Identify the blood parasite species.
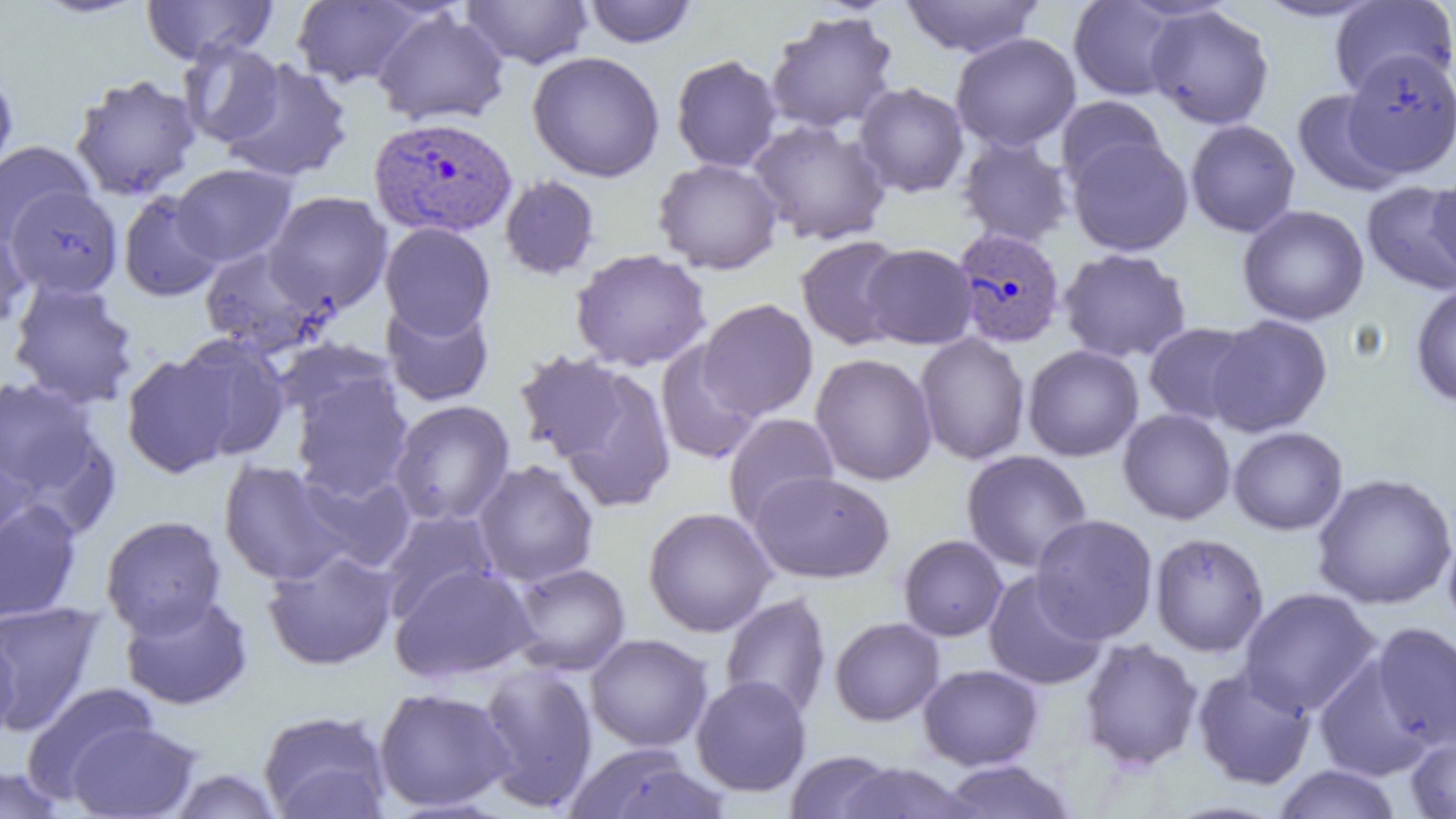
Plasmodium vivax.

Summary:
  - Coordinate format: approximate bounding boxes as (x1,y1)-(x2,y2) corner pairs in pixels
  - Uninfected red blood cell locations: (27,0)-(151,19), (140,0)-(278,65), (291,0)-(427,89), (460,0)-(594,69), (900,0)-(1044,58), (1250,0)-(1387,22), (584,1)-(698,48), (1068,1)-(1185,101), (1329,1)-(1456,98), (1145,4)-(1275,130), (371,9)-(510,127), (765,11)-(899,135), (950,33)-(1081,152), (179,39)-(286,148), (527,50)-(665,182), (1342,51)-(1455,177), (671,54)-(782,173), (220,59)-(353,182), (0,69)-(18,184), (70,74)-(202,201), (854,82)-(969,197), (1292,89)-(1405,196), (1056,95)-(1165,189), (1185,119)-(1300,238), (748,120)-(891,245), (958,136)-(1074,246), (1067,137)-(1194,256), (0,140)-(94,249), (653,158)-(783,274), (171,163)-(297,267), (1427,169)-(1456,283), (499,175)-(600,281), (1361,181)-(1456,296), (4,188)-(126,298), (118,191)-(223,302), (264,191)-(393,315), (1237,204)-(1369,326), (0,216)-(32,334), (380,223)-(496,339), (795,235)-(909,350), (861,243)-(977,349), (199,247)-(326,356), (570,248)-(712,371), (1058,248)-(1192,363), (8,279)-(140,409), (1410,282)-(1456,408), (698,298)-(818,421), (381,299)-(494,407), (1206,314)-(1333,437), (1143,322)-(1255,425), (915,333)-(1031,465), (173,334)-(291,460), (273,338)-(398,429), (655,341)-(763,465), (1023,344)-(1144,461), (513,350)-(630,463), (121,352)-(239,478), (810,353)-(938,486), (558,368)-(677,513), (292,374)-(413,501), (0,376)-(107,507), (388,399)-(515,526), (1118,408)-(1236,524), (723,413)-(839,529), (1228,426)-(1348,535), (0,439)-(33,558), (961,449)-(1093,573), (473,459)-(599,587), (219,460)-(354,586), (296,466)-(417,573), (750,470)-(894,583), (1312,472)-(1456,610), (0,499)-(81,623), (643,507)-(777,637), (379,508)-(500,621), (100,514)-(226,638), (1030,514)-(1158,643), (1442,528)-(1456,639), (1150,532)-(1270,657), (898,535)-(1007,641), (262,547)-(400,670), (390,563)-(538,683), (509,563)-(631,676), (982,570)-(1108,691), (1238,587)-(1380,717), (120,593)-(253,710), (720,593)-(831,719), (0,600)-(107,736), (830,617)-(944,726), (1369,622)-(1456,751), (0,623)-(19,747), (586,633)-(713,752), (1079,637)-(1203,772), (1313,654)-(1434,781), (477,664)-(599,812), (918,664)-(1043,770), (1192,666)-(1317,790), (690,675)-(812,797), (22,682)-(159,800), (373,687)-(514,813), (258,709)-(392,819), (66,722)-(201,819), (1405,734)-(1456,818), (562,743)-(728,819), (785,749)-(900,819), (937,759)-(1077,818), (832,761)-(976,819), (0,764)-(70,818), (1272,764)-(1402,819), (169,767)-(284,819)
  - Plasmodium vivax-infected red blood cell locations: (368,115)-(517,239), (952,226)-(1066,349)
  - Preparation: thin blood smear
  - Modality: light microscopy
  - Magnification: 1000x
  - Image size: 1456×819 pixels
  - Field of view: single